Give the position of every Plasmodium falciparum parasite, noting its life-cycle stage.
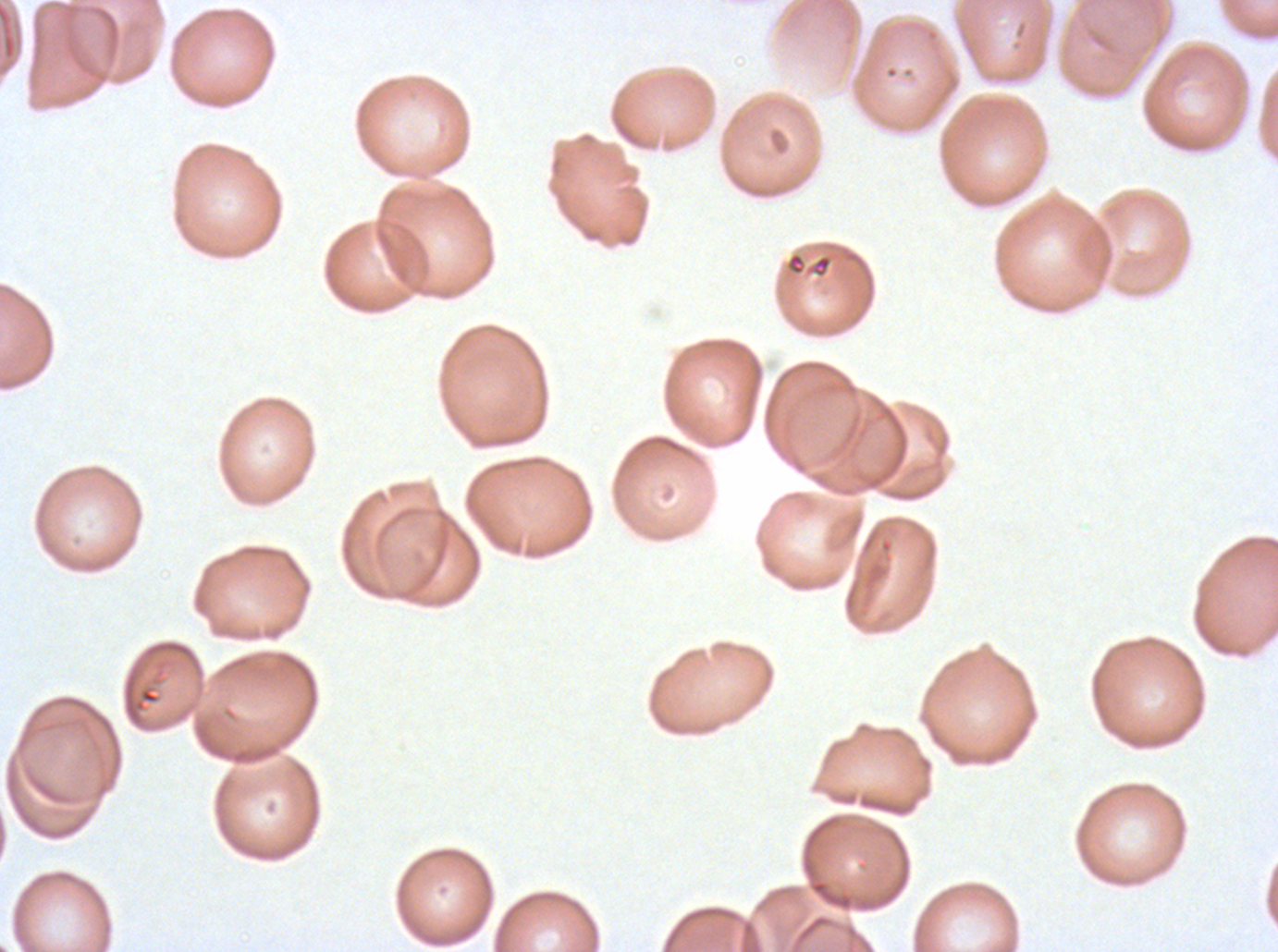

No rings, late-ring/early-trophozoite forms, mid trophozoites, late trophozoites, early schizonts, late schizonts, segmenters, or gametocytes observed.

Approximate bounding boxes as {x1, y1, x2, y2} in pixels.
Summary:
  - Debris locations: {785, 251, 833, 279}
  - Image size: 1278×952 pixels
  - Field of view: one sub-image of a larger composite
  - Specimen: Plasmodium falciparum cultured ex vivo for 24 to 48 hours, from a patient in The Gambia
  - Stain: Giemsa
  - Preparation: thin blood film